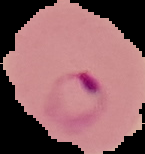
Summary:
  - Image type: segmented cell region with the area outside set to black
  - Image size: 145×154 pixels
  - Result: malaria parasites identified
  - Preparation: thin blood film